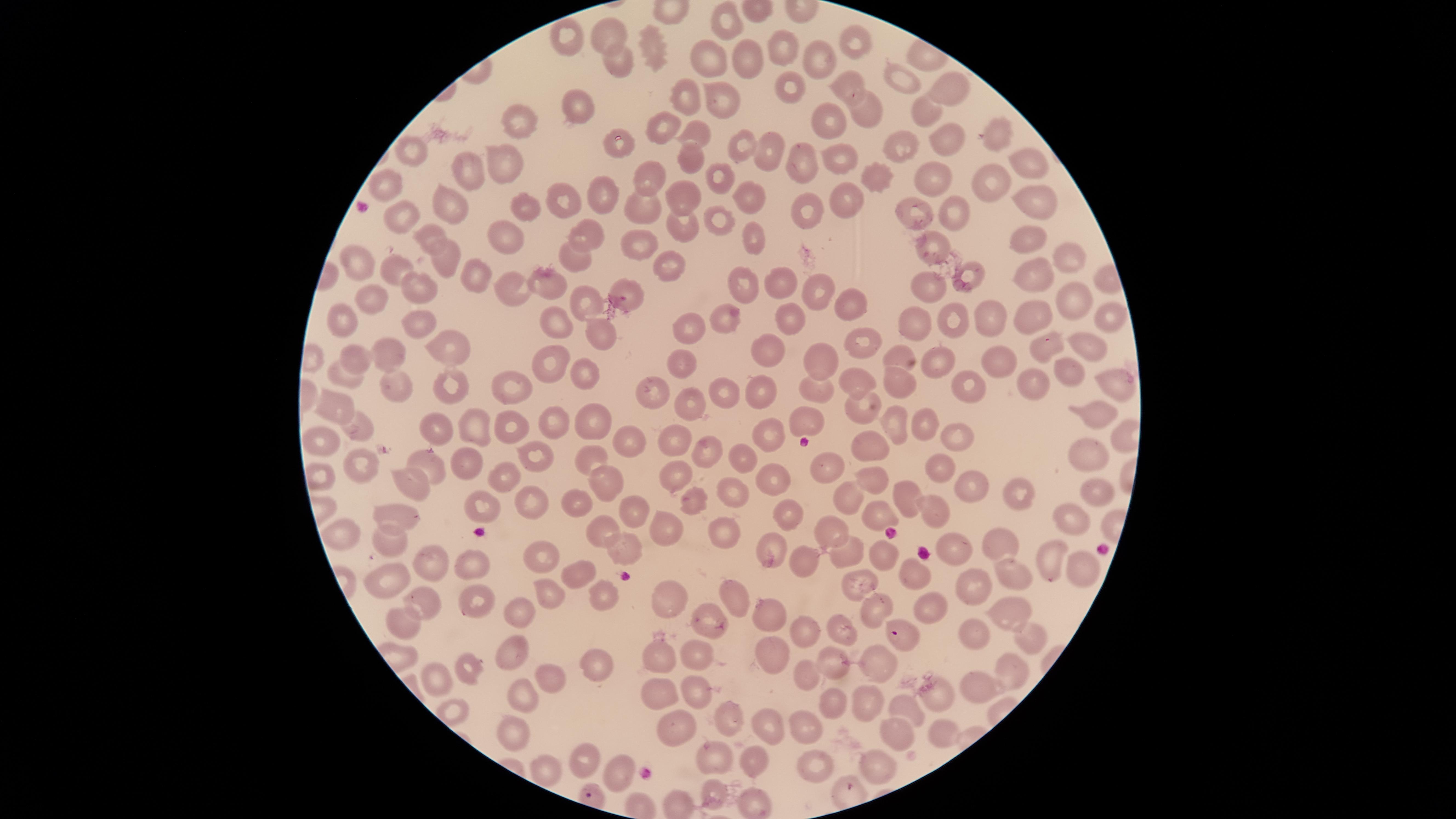

preparation = thin blood film
visible region = circular
species = Plasmodium falciparum
parasitized red blood cells = approximate marker points as [x, y] in pixels: [902, 633]
capture = smartphone photograph through the microscope eyepiece
field of view = single
uninfected red blood cells = approximate marker points as [x, y] in pixels: [723, 20], [610, 32], [564, 34], [652, 39], [854, 39], [781, 47], [738, 55], [614, 57], [819, 57], [711, 58], [841, 80], [903, 81], [785, 84], [951, 86], [721, 94], [683, 100], [581, 105], [869, 105], [926, 111], [515, 118], [833, 120], [663, 123], [697, 135], [952, 139], [994, 139], [621, 144], [906, 144], [741, 145], [415, 146], [769, 147], [845, 152], [801, 153], [688, 154], [500, 157], [465, 166], [1025, 166], [716, 171], [876, 177], [934, 177], [990, 178], [651, 181], [388, 183], [604, 191], [692, 192], [746, 195], [1039, 198], [565, 199], [844, 200], [449, 203], [526, 204], [644, 205], [811, 206], [918, 210], [955, 211], [713, 216], [403, 217], [681, 224], [588, 232], [430, 233], [507, 233], [1032, 235], [749, 237], [927, 238], [635, 239], [1064, 255], [444, 256], [576, 258], [668, 261], [352, 262], [390, 268], [1026, 274], [474, 278], [970, 279], [742, 282], [549, 283], [510, 284], [779, 284], [412, 285], [925, 285], [626, 287], [1073, 293], [818, 295], [373, 297], [583, 298], [851, 305], [1108, 311], [728, 314], [1035, 314], [550, 317], [987, 319], [348, 320], [801, 320], [948, 320], [914, 322], [423, 323], [689, 329], [606, 331], [863, 337], [1091, 345], [764, 348], [1046, 350], [390, 351], [452, 352], [355, 354], [896, 358], [552, 360], [940, 360], [993, 360], [820, 361], [673, 364], [1065, 368], [580, 369], [342, 376], [859, 380], [902, 380], [392, 381], [510, 385], [1117, 385], [816, 387], [649, 388], [763, 388], [970, 388], [1034, 388], [726, 391], [455, 393], [694, 400], [856, 406], [337, 407], [1096, 410], [550, 417], [805, 417], [926, 422], [592, 423], [894, 423], [360, 426], [435, 426], [477, 426], [513, 427], [765, 431], [319, 437], [959, 439], [624, 441], [671, 441], [873, 444], [1088, 448], [705, 449], [737, 453], [533, 456], [821, 458], [354, 460], [429, 462], [466, 462], [592, 462], [940, 470], [872, 475], [403, 477], [499, 477], [676, 477], [773, 477], [606, 478], [972, 483], [1097, 484], [734, 488], [905, 489], [1010, 489], [841, 494], [534, 495], [690, 498], [579, 502], [635, 506], [1069, 508], [934, 509], [481, 511], [883, 511], [785, 514], [409, 515], [668, 528], [836, 528], [723, 530], [602, 531], [341, 535], [390, 539], [1001, 541], [773, 542], [883, 545], [619, 546], [958, 551], [845, 552], [536, 555], [433, 557], [802, 562], [1008, 566], [1047, 566], [911, 567], [1079, 567], [469, 568], [578, 573], [388, 577], [856, 580], [975, 588], [553, 589], [597, 596], [735, 596], [663, 598], [932, 599], [469, 600], [423, 601], [869, 602], [523, 609], [765, 613], [1008, 613], [705, 617], [400, 622], [841, 628], [803, 629], [975, 630], [1029, 630], [513, 643], [770, 651], [654, 656], [689, 658], [877, 661], [595, 665], [833, 665], [464, 670], [803, 672], [1010, 672], [547, 681], [438, 683], [693, 686], [518, 687], [659, 691], [971, 692], [829, 699], [864, 700], [902, 706], [731, 717], [683, 721], [764, 721], [809, 730], [939, 732], [891, 733], [513, 734], [584, 755], [718, 758], [751, 758], [816, 760], [875, 761], [610, 772], [545, 773], [713, 793], [755, 799]
presence = malaria parasites identified
stain = Giemsa
image size = 1456×819 pixels